Assess this cell for malaria.
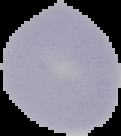

It is uninfected.

Summary:
  - Preparation: thin blood smear
  - Image type: segmented cell region on a black background
  - Image size: 121×136 pixels